Give the extent of all Trypanosoma brucei.
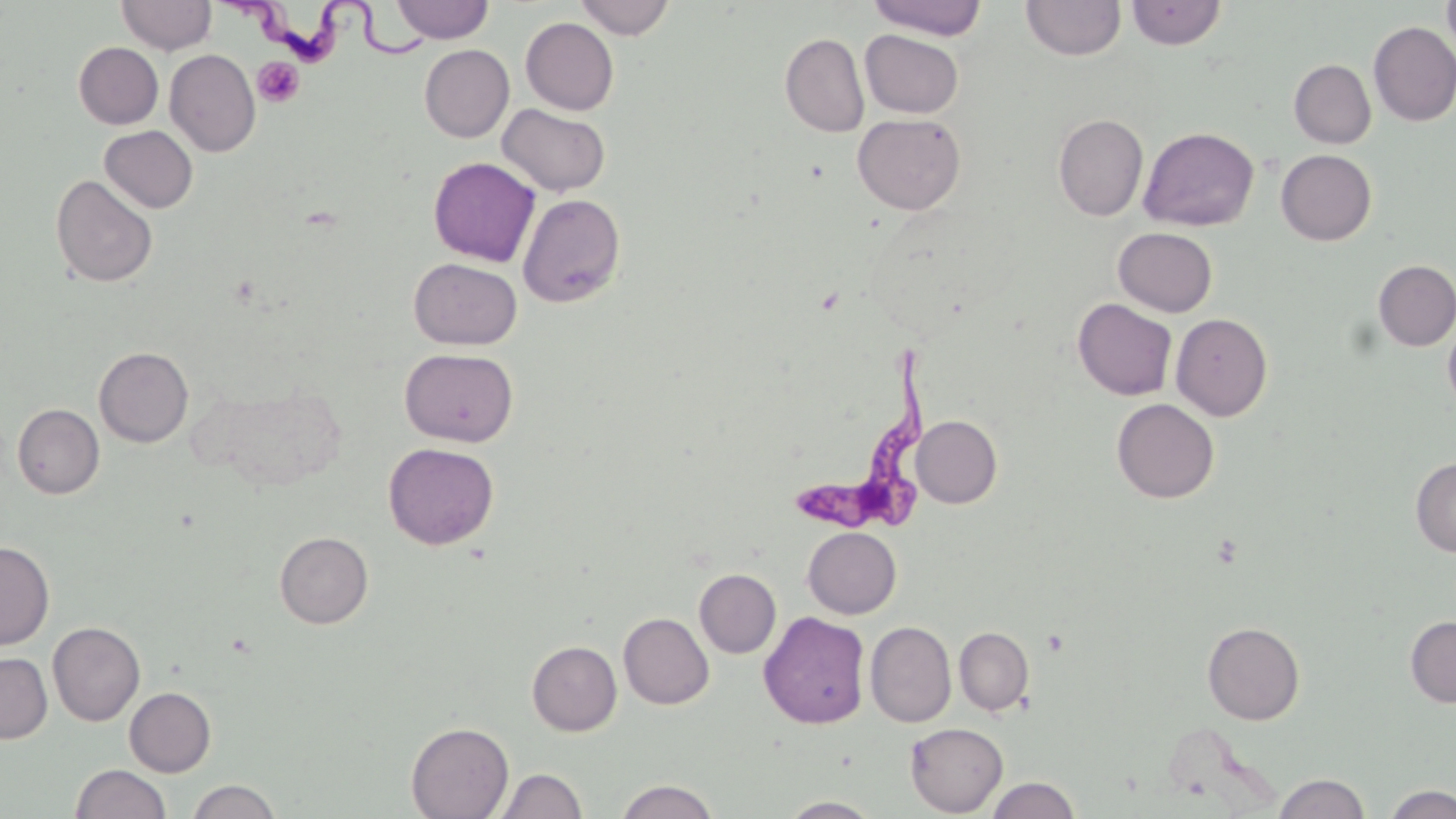

Approximate bounding boxes as named x1/y1/x2/y2 corners in pixels.
Trypanosoma brucei: (x1=222, y1=0, x2=430, y2=64), (x1=799, y1=336, x2=944, y2=532).

Summary:
  - Platelet locations: (x1=252, y1=56, x2=304, y2=108)
  - Uninfected red blood cell locations: (x1=117, y1=0, x2=217, y2=55), (x1=574, y1=0, x2=675, y2=39), (x1=866, y1=0, x2=988, y2=39), (x1=1021, y1=0, x2=1125, y2=60), (x1=1442, y1=0, x2=1456, y2=60), (x1=391, y1=1, x2=493, y2=43), (x1=1126, y1=1, x2=1226, y2=49), (x1=520, y1=17, x2=619, y2=115), (x1=1368, y1=21, x2=1456, y2=126), (x1=860, y1=29, x2=964, y2=118), (x1=780, y1=32, x2=870, y2=137), (x1=74, y1=42, x2=163, y2=129), (x1=419, y1=44, x2=514, y2=142), (x1=164, y1=49, x2=260, y2=156), (x1=1289, y1=59, x2=1376, y2=148), (x1=497, y1=103, x2=611, y2=196), (x1=852, y1=113, x2=966, y2=215), (x1=1053, y1=114, x2=1148, y2=220), (x1=100, y1=125, x2=198, y2=213), (x1=1139, y1=126, x2=1259, y2=232), (x1=1276, y1=149, x2=1376, y2=245), (x1=428, y1=156, x2=541, y2=267), (x1=50, y1=174, x2=158, y2=288), (x1=517, y1=193, x2=625, y2=308), (x1=1113, y1=227, x2=1217, y2=317), (x1=408, y1=258, x2=522, y2=350), (x1=1373, y1=260, x2=1456, y2=351), (x1=1073, y1=298, x2=1177, y2=400), (x1=1171, y1=313, x2=1273, y2=421), (x1=1442, y1=316, x2=1456, y2=415), (x1=94, y1=346, x2=193, y2=447), (x1=399, y1=347, x2=519, y2=447), (x1=203, y1=381, x2=347, y2=490), (x1=1112, y1=398, x2=1219, y2=503), (x1=12, y1=403, x2=104, y2=499), (x1=911, y1=415, x2=1002, y2=508), (x1=383, y1=442, x2=499, y2=549), (x1=1411, y1=457, x2=1456, y2=556), (x1=802, y1=526, x2=901, y2=618), (x1=274, y1=531, x2=373, y2=628), (x1=0, y1=541, x2=54, y2=650), (x1=693, y1=568, x2=781, y2=658), (x1=759, y1=610, x2=871, y2=729), (x1=618, y1=612, x2=714, y2=709), (x1=1405, y1=616, x2=1456, y2=707), (x1=48, y1=621, x2=145, y2=726), (x1=865, y1=621, x2=956, y2=727), (x1=1202, y1=622, x2=1305, y2=725), (x1=954, y1=625, x2=1034, y2=715), (x1=527, y1=640, x2=622, y2=736), (x1=0, y1=652, x2=52, y2=743), (x1=124, y1=687, x2=216, y2=776), (x1=406, y1=722, x2=514, y2=819), (x1=905, y1=723, x2=1008, y2=816), (x1=71, y1=764, x2=171, y2=819), (x1=493, y1=768, x2=588, y2=818), (x1=1273, y1=773, x2=1370, y2=818), (x1=985, y1=776, x2=1081, y2=819), (x1=186, y1=779, x2=282, y2=819), (x1=615, y1=779, x2=719, y2=819), (x1=1383, y1=784, x2=1456, y2=819), (x1=779, y1=796, x2=883, y2=818)
  - Slide-level diagnosis: Trypanosoma brucei
  - Stain: May-Grünwald-Giemsa
  - Field of view: single
  - Preparation: thin blood smear
  - Modality: light microscopy
  - Magnification: 1000x
  - Image size: 1456×819 pixels